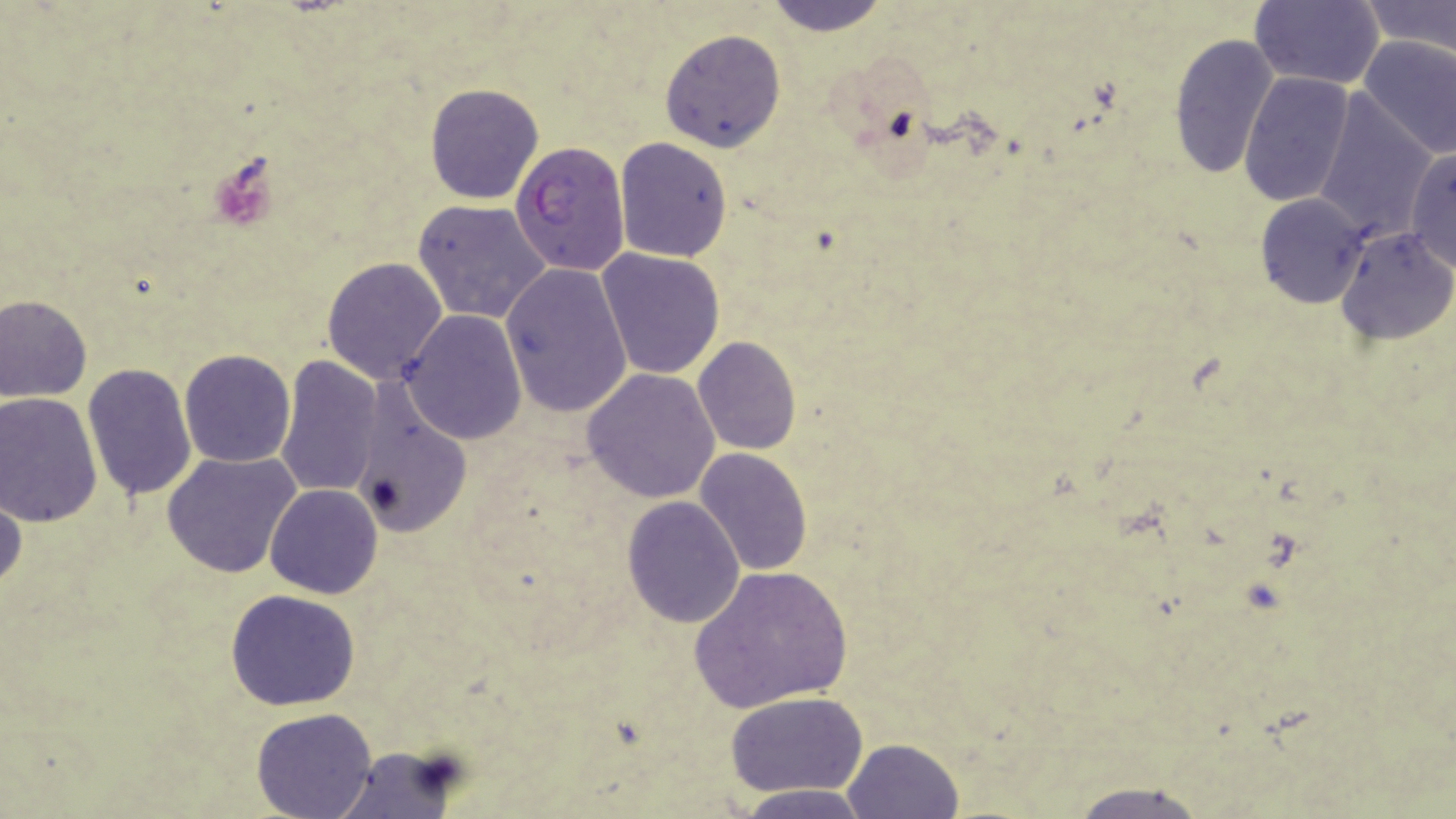
Approximate bounding boxes as [x1, y1, x2, y2] in pixels. Uninfected red blood cell locations: [763, 0, 891, 34], [1251, 0, 1386, 90], [1360, 0, 1455, 55], [660, 29, 786, 152], [1169, 33, 1279, 183], [1357, 35, 1456, 159], [1240, 72, 1355, 208], [425, 82, 545, 205], [1314, 95, 1437, 240], [613, 136, 734, 262], [1404, 146, 1456, 272], [1256, 193, 1370, 308], [411, 198, 554, 324], [1336, 227, 1455, 344], [597, 248, 726, 379], [321, 256, 449, 385], [500, 261, 633, 418], [0, 294, 93, 403], [399, 310, 527, 444], [693, 336, 802, 455], [178, 350, 296, 467], [273, 354, 384, 500], [82, 363, 197, 502], [582, 368, 720, 503], [350, 379, 474, 536], [0, 391, 103, 526], [695, 447, 813, 577], [161, 450, 301, 579], [252, 484, 375, 707], [265, 484, 382, 598], [0, 489, 25, 599], [622, 495, 745, 628], [689, 564, 855, 714], [226, 589, 361, 711], [726, 692, 869, 797], [251, 708, 379, 819], [844, 738, 963, 817], [330, 747, 464, 819], [1062, 780, 1220, 819], [733, 785, 870, 817]. Plasmodium falciparum-infected red blood cell locations: [510, 140, 630, 277]. Slide-level diagnosis: Plasmodium falciparum. 1000x magnification. One field of a larger specimen. Image is 1456×819 pixels. Optical microscopy. May-Grünwald-Giemsa-stained preparation. Thin blood film.